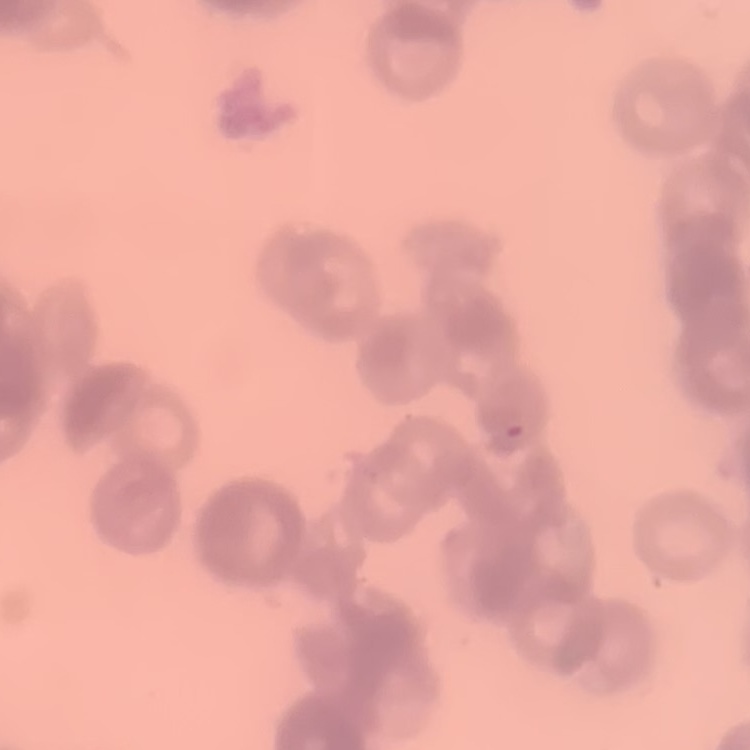

erythrocyte morphology = rouleaux formation
preparation = thin blood smear
image type = square crop of a larger photomicrograph
stain = Field's or Giemsa